Assess the morphology of the erythrocytes.
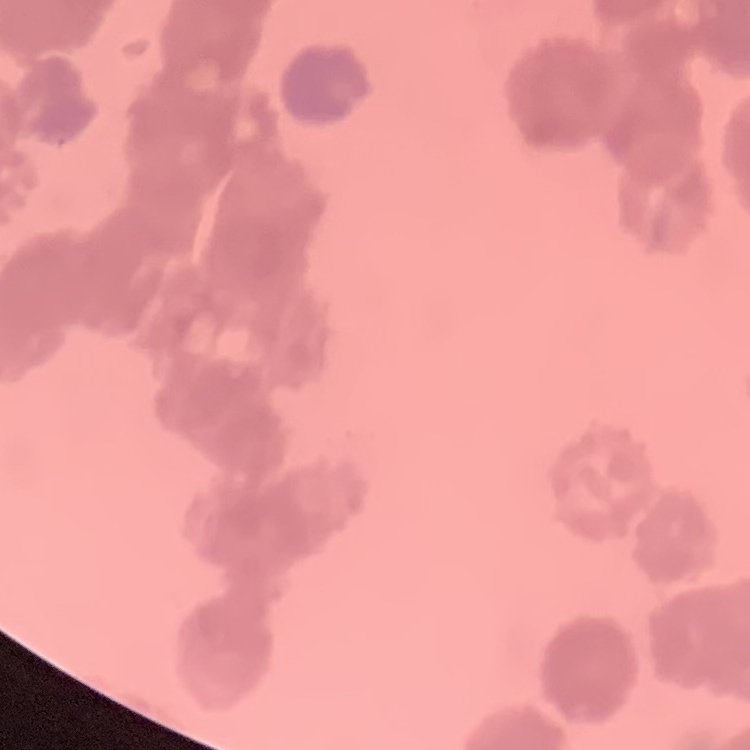
Rouleaux formation.

preparation: thin blood smear
image_type: one tile cut from a larger photomicrograph
stain: Field's or Giemsa